Assess this cell for malaria.
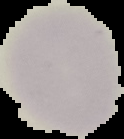
Uninfected.

{
  "image_size": "124×139 pixels",
  "image_type": "segmented cell region with the area outside set to black",
  "preparation": "thin blood smear"
}